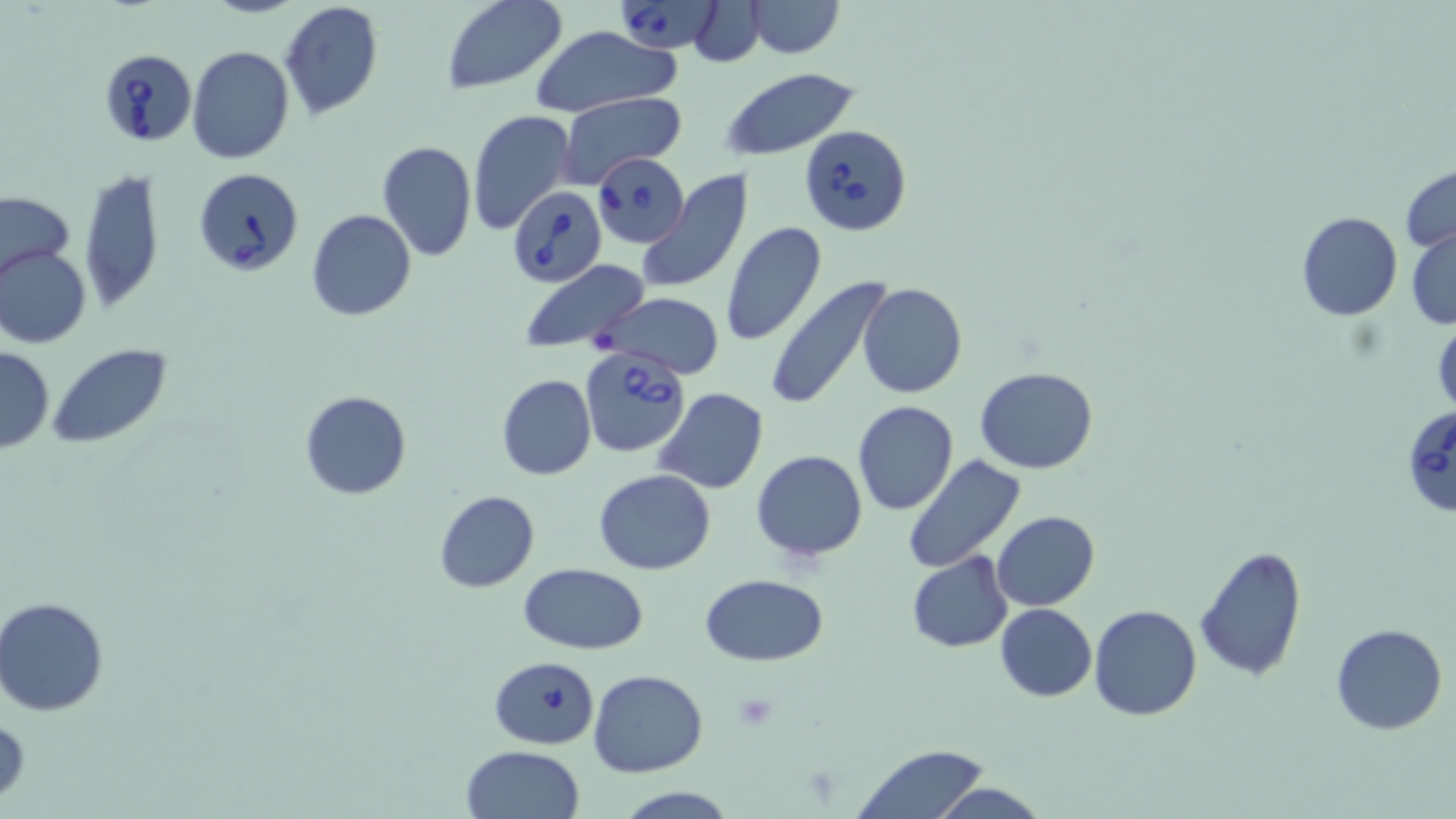
Summary:
  - Coordinate format: approximate bounding boxes as [x1, y1, x2, y2] in pixels
  - Babesia divergens-infected red blood cell locations: [617, 1, 722, 52], [98, 48, 198, 145], [799, 124, 914, 236], [597, 152, 687, 249], [194, 167, 304, 278], [506, 187, 607, 287], [576, 345, 690, 458], [1401, 404, 1456, 518]
  - Uninfected red blood cell locations: [440, 0, 568, 96], [743, 0, 845, 58], [278, 1, 385, 120], [686, 3, 769, 64], [527, 25, 682, 118], [187, 46, 295, 165], [721, 69, 859, 160], [558, 92, 686, 185], [466, 109, 575, 236], [376, 140, 477, 261], [1400, 164, 1456, 254], [78, 167, 166, 311], [635, 169, 754, 295], [1, 190, 77, 287], [306, 209, 416, 322], [1296, 211, 1402, 321], [720, 222, 826, 348], [1406, 227, 1456, 330], [1, 245, 92, 348], [517, 259, 653, 357], [764, 275, 896, 410], [858, 284, 967, 399], [598, 292, 724, 379], [1431, 319, 1456, 419], [49, 344, 173, 449], [0, 346, 54, 453], [975, 367, 1099, 474], [496, 374, 597, 480], [652, 387, 770, 495], [300, 390, 411, 500], [851, 400, 960, 515], [752, 450, 868, 562], [902, 457, 1026, 574], [593, 470, 717, 575], [433, 490, 540, 593], [992, 510, 1099, 612], [1192, 544, 1309, 682], [905, 550, 1013, 653], [516, 561, 649, 654], [701, 574, 829, 666], [1, 597, 113, 716], [995, 602, 1097, 702], [1088, 605, 1202, 720], [1332, 624, 1447, 734], [490, 656, 600, 750], [589, 670, 708, 777], [0, 713, 29, 806], [852, 742, 992, 819], [460, 745, 584, 819], [928, 783, 1049, 819], [611, 786, 742, 818]
  - Platelet locations: [731, 693, 779, 733]
  - Slide-level diagnosis: Babesia divergens
  - Stain: May-Grünwald-Giemsa
  - Modality: optical microscopy
  - Preparation: thin blood smear
  - Field of view: single
  - Magnification: 1000x
  - Image size: 1456×819 pixels